Report the malaria status of this cell.
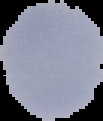
It is parasitized.

Summary:
  - Image size: 103×121 pixels
  - Preparation: thin blood smear
  - Image type: segmented cell region with the area outside set to black